State which parasite is depicted.
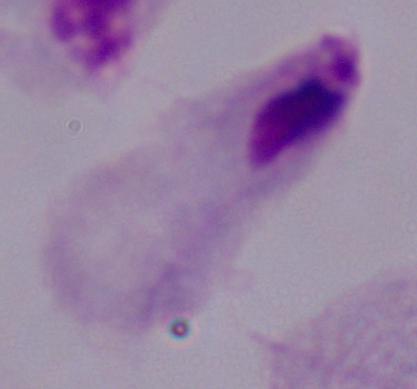
A trichomonad.

magnification: 1000x
modality: photomicrograph